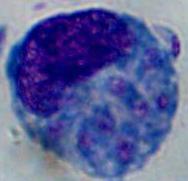

Summary:
  - Modality: micrograph
  - Magnification: 1000x
  - Identification: leukocyte